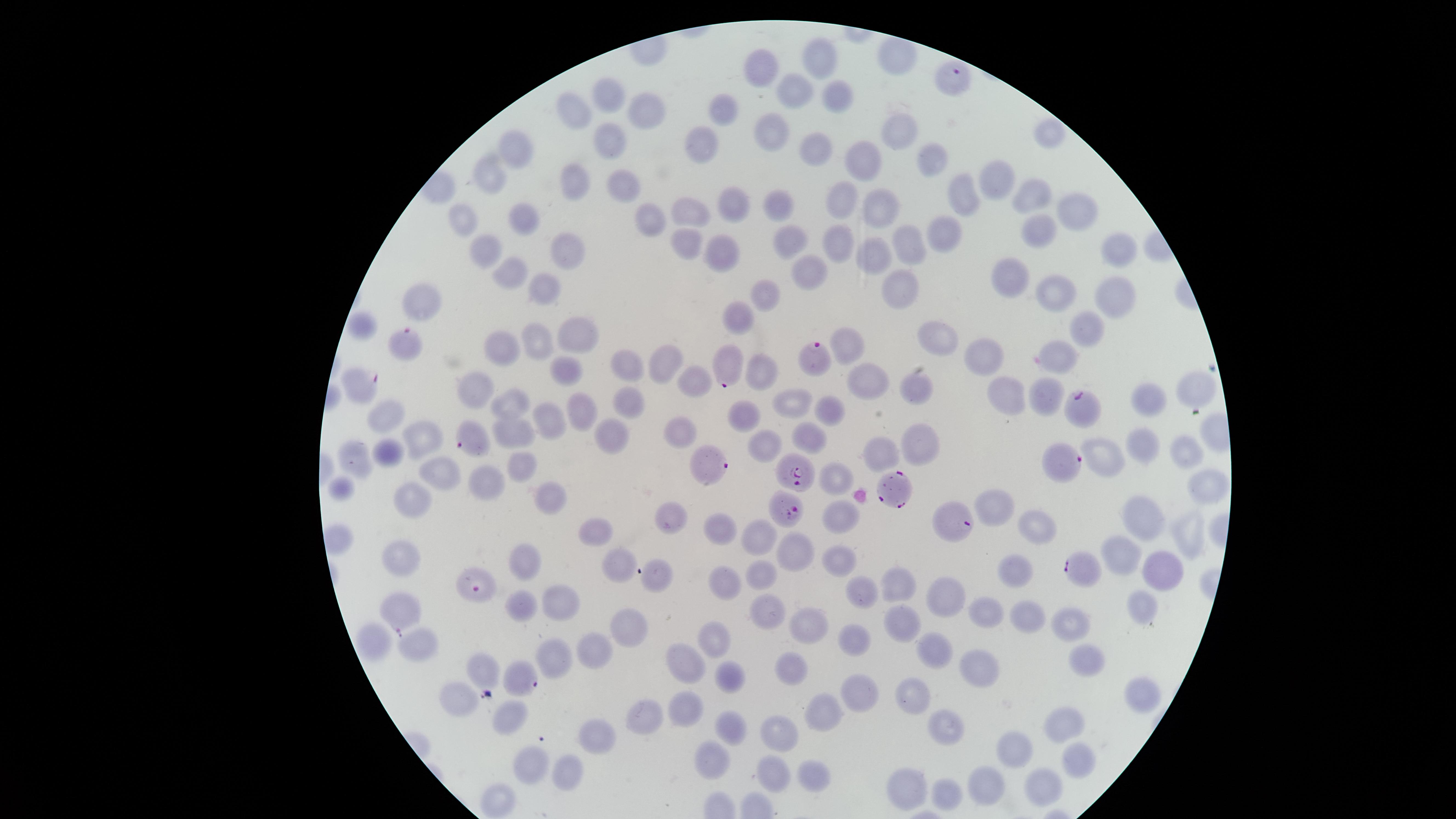 Approximate marker points as [x, y] in pixels. Parasitized red blood cells: [950, 81], [400, 339], [815, 357], [728, 364], [351, 380], [1079, 409], [474, 437], [1062, 464], [707, 465], [802, 477], [890, 487], [786, 507], [947, 521], [1072, 567], [478, 587], [401, 613], [523, 679]. Uninfected red blood cells: [899, 56], [822, 58], [763, 69], [800, 86], [611, 94], [832, 95], [578, 101], [724, 109], [648, 110], [774, 125], [903, 129], [1049, 132], [606, 134], [706, 139], [815, 145], [518, 154], [868, 154], [936, 163], [494, 171], [578, 175], [624, 182], [995, 182], [1034, 193], [845, 196], [963, 198], [730, 199], [781, 200], [882, 201], [694, 207], [467, 209], [1084, 213], [650, 215], [525, 217], [1039, 228], [947, 233], [686, 239], [909, 242], [788, 243], [845, 243], [572, 244], [482, 246], [1119, 248], [723, 249], [880, 256], [510, 268], [810, 268], [1013, 278], [543, 285], [901, 287], [769, 291], [1056, 292], [1116, 293], [424, 301], [742, 311], [1090, 324], [362, 326], [577, 332], [938, 334], [535, 339], [849, 342], [504, 344], [986, 355], [1062, 357], [664, 362], [626, 367], [756, 370], [568, 375], [697, 377], [869, 379], [916, 383], [474, 386], [1005, 387], [1193, 387], [1044, 390], [1150, 392], [512, 401], [790, 405], [631, 407], [831, 408], [583, 413], [742, 416], [387, 420], [555, 422], [682, 429], [514, 434], [608, 435], [420, 436], [806, 436], [918, 443], [1141, 446], [765, 448], [389, 449], [1185, 451], [885, 454], [355, 456], [1108, 461], [524, 463], [433, 469], [485, 478], [840, 482], [1207, 485], [344, 487], [550, 497], [408, 504], [999, 505], [841, 513], [1148, 515], [668, 518], [1031, 526], [1190, 528], [719, 529], [601, 531], [760, 537], [793, 549], [1123, 555], [620, 561], [398, 563], [525, 563], [834, 563], [1157, 567], [760, 570], [657, 573], [1017, 575], [722, 577], [894, 589], [947, 594], [864, 596], [559, 599], [519, 600], [765, 607], [1143, 608], [991, 610], [1026, 613], [812, 622], [1077, 623], [631, 627], [901, 631], [422, 637], [378, 639], [854, 639], [716, 640], [599, 649], [556, 653], [938, 653], [689, 654], [1085, 657], [493, 665], [790, 665], [974, 672], [734, 674], [913, 689], [856, 692], [1142, 693], [464, 694], [648, 707], [689, 707], [514, 710], [822, 714], [1072, 720], [735, 726], [782, 727], [944, 728], [599, 732], [1017, 750], [1073, 754], [710, 756], [532, 763], [563, 769], [770, 770], [800, 779], [907, 780], [991, 780], [1037, 788], [953, 790], [505, 799]. Image is 1456×819 pixels. The visible region is circular. Smartphone photograph through the microscope eyepiece. Species: Plasmodium falciparum. Giemsa stain. Thin smear of blood. Presence: malaria parasites detected. One field of view of the specimen.